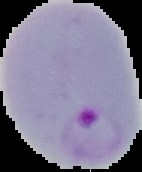 Image is 142×172 pixels. From a thin blood film. The area outside the segmented cell region is set to black. Result: malaria parasites detected.